Classify this cell by malaria status.
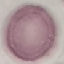

Uninfected.

{
  "image_type": "cell patch, automatically extracted from a larger field of view and resized to 64 × 64 pixels",
  "preparation": "thin smear",
  "capture": "smartphone camera at the microscope eyepiece",
  "stain": "Giemsa"
}